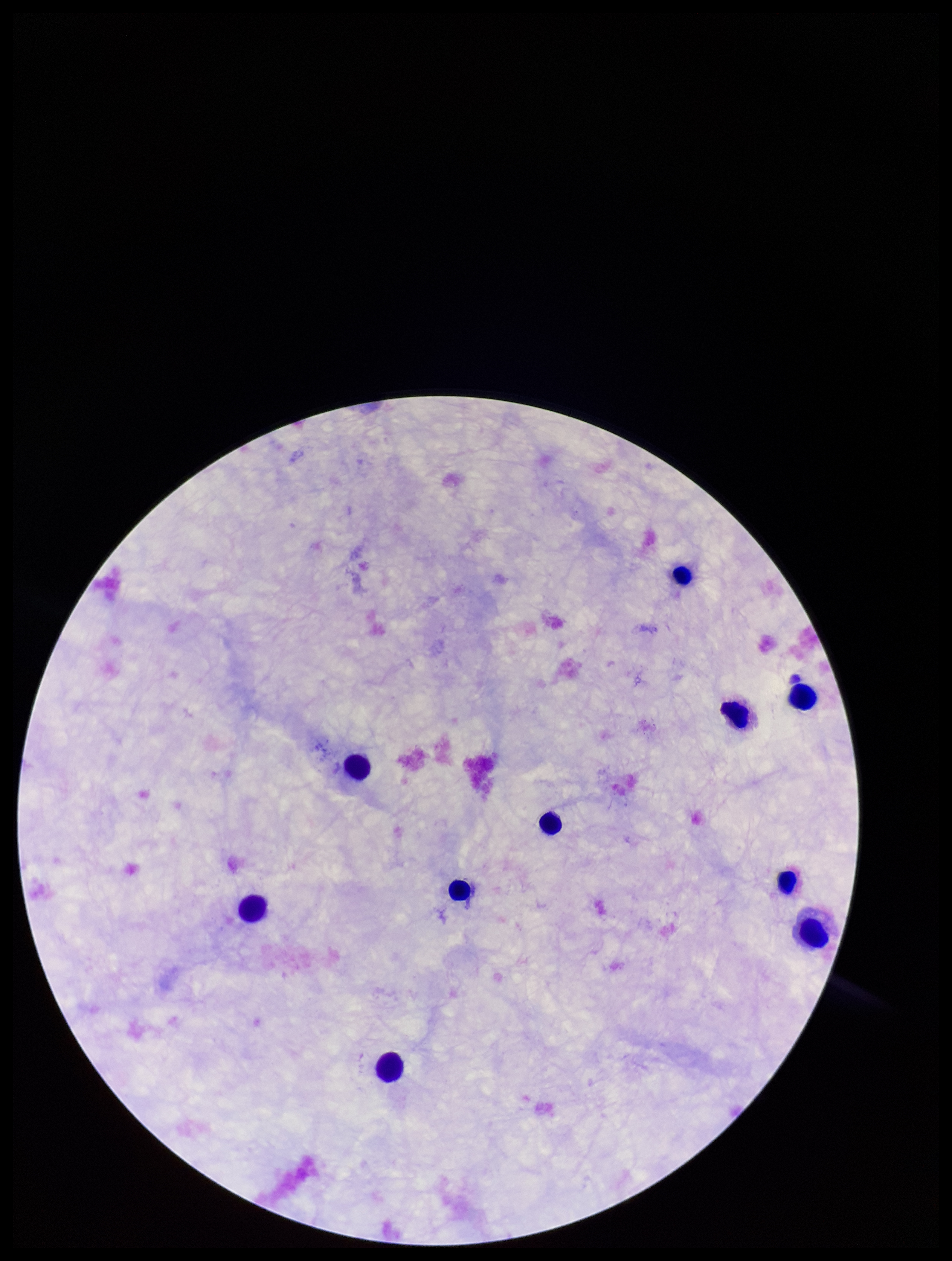
Summary:
  - Plasmodium parasites: none identified
  - Leukocyte count: 10
  - Image size: 952×1261 pixels
  - Capture: smartphone photograph through the microscope eyepiece
  - Parasite count: 0
  - Patient malaria status: negative
  - Field of view: one from this slide
  - Stain: Giemsa
  - Preparation: thick